Outline each blood parasite and name the species.
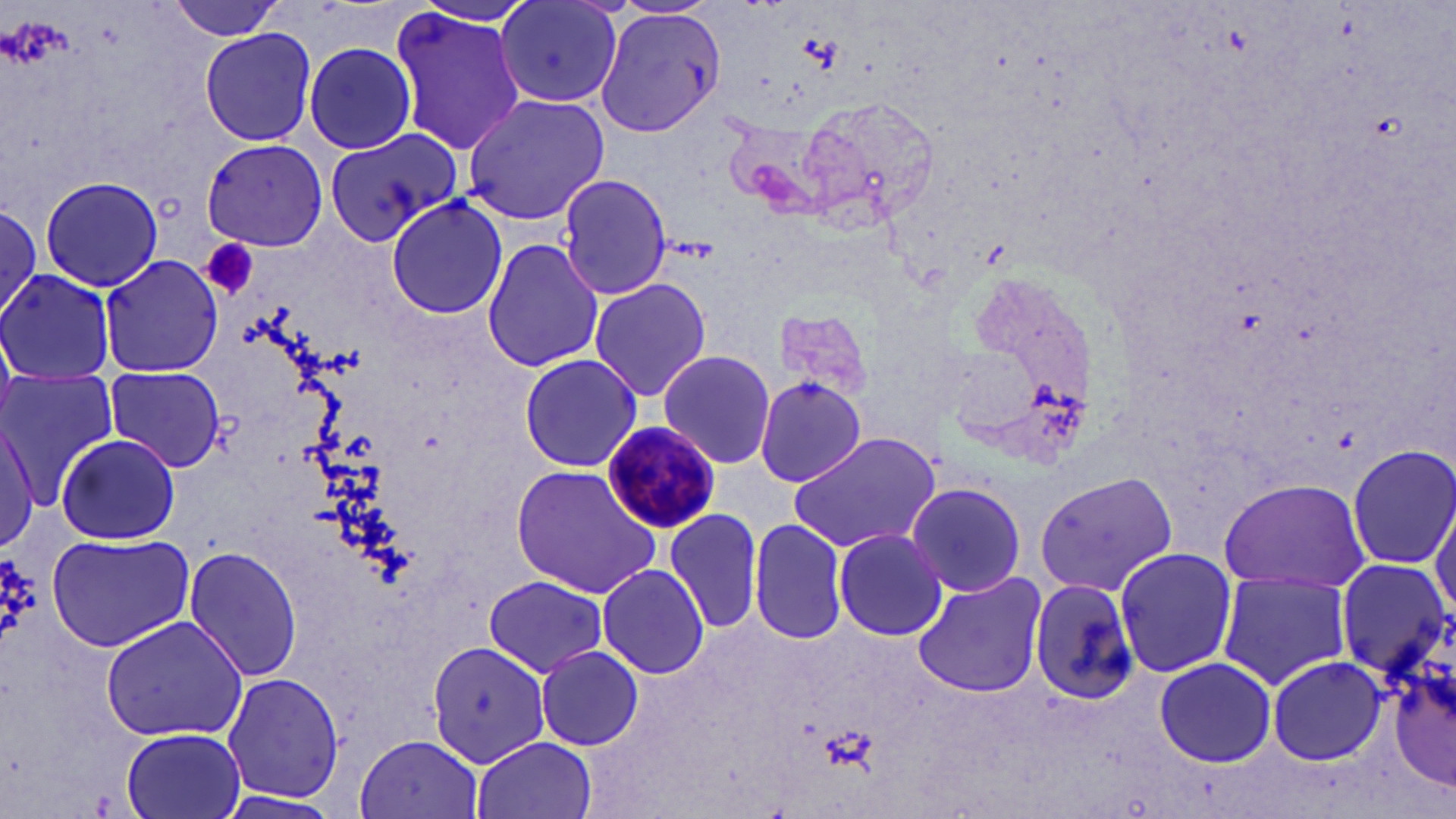
Approximate bounding boxes as named x1/y1/x2/y2 corners in pixels.
Plasmodium malariae-infected red blood cells: (x1=599, y1=419, x2=722, y2=536).
No Plasmodium falciparum, Plasmodium ovale, Plasmodium vivax, Babesia divergens, or Trypanosoma brucei observed.

Summary:
  - Uninfected red blood cell locations: (x1=165, y1=0, x2=293, y2=42), (x1=491, y1=0, x2=626, y2=105), (x1=495, y1=0, x2=621, y2=107), (x1=389, y1=6, x2=524, y2=158), (x1=593, y1=7, x2=725, y2=138), (x1=198, y1=27, x2=319, y2=149), (x1=303, y1=42, x2=417, y2=156), (x1=461, y1=93, x2=610, y2=224), (x1=797, y1=96, x2=943, y2=234), (x1=323, y1=128, x2=460, y2=246), (x1=200, y1=138, x2=329, y2=251), (x1=557, y1=171, x2=672, y2=300), (x1=38, y1=176, x2=162, y2=294), (x1=386, y1=198, x2=509, y2=318), (x1=0, y1=203, x2=42, y2=323), (x1=480, y1=237, x2=604, y2=374), (x1=95, y1=253, x2=225, y2=378), (x1=0, y1=269, x2=118, y2=385), (x1=586, y1=276, x2=712, y2=404), (x1=767, y1=304, x2=877, y2=407), (x1=518, y1=351, x2=644, y2=474), (x1=658, y1=351, x2=778, y2=468), (x1=103, y1=367, x2=226, y2=473), (x1=1, y1=370, x2=119, y2=505), (x1=756, y1=375, x2=869, y2=489), (x1=0, y1=416, x2=39, y2=558), (x1=788, y1=432, x2=941, y2=552), (x1=55, y1=434, x2=182, y2=546), (x1=1347, y1=444, x2=1455, y2=571), (x1=511, y1=465, x2=663, y2=597), (x1=1032, y1=469, x2=1178, y2=598), (x1=1215, y1=477, x2=1372, y2=595), (x1=905, y1=480, x2=1026, y2=598), (x1=1430, y1=499, x2=1455, y2=623), (x1=664, y1=507, x2=762, y2=634), (x1=747, y1=517, x2=848, y2=644), (x1=832, y1=527, x2=949, y2=641), (x1=46, y1=533, x2=194, y2=651), (x1=184, y1=544, x2=303, y2=684), (x1=1112, y1=546, x2=1238, y2=681), (x1=1333, y1=557, x2=1452, y2=679), (x1=598, y1=562, x2=709, y2=679), (x1=1216, y1=571, x2=1355, y2=690), (x1=910, y1=572, x2=1047, y2=699), (x1=482, y1=575, x2=611, y2=677), (x1=1026, y1=577, x2=1140, y2=707), (x1=98, y1=613, x2=248, y2=742), (x1=1385, y1=628, x2=1454, y2=797), (x1=429, y1=641, x2=547, y2=767), (x1=535, y1=645, x2=644, y2=752), (x1=1266, y1=654, x2=1390, y2=767), (x1=1152, y1=656, x2=1278, y2=768), (x1=222, y1=673, x2=343, y2=801), (x1=120, y1=728, x2=248, y2=819), (x1=355, y1=733, x2=483, y2=818), (x1=474, y1=735, x2=597, y2=819), (x1=210, y1=791, x2=341, y2=819)
  - Platelet locations: (x1=200, y1=238, x2=261, y2=302)
  - Slide-level diagnosis: Plasmodium malariae
  - Modality: optical microscopy
  - Field of view: one of a larger specimen
  - Magnification: 1000x
  - Preparation: thin blood film
  - Stain: May-Grünwald-Giemsa
  - Image size: 1456×819 pixels